Report the malaria status of this cell.
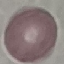

Uninfected.

Automatically extracted cell patch, resized to 64 × 64 pixels. Acquired by smartphone through the microscope eyepiece. Giemsa stain. Thin smear of blood.